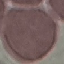

Result: no malaria parasites seen. Giemsa stain. Acquired by smartphone through the microscope eyepiece. Cell patch, automatically extracted from a larger field of view and resized to 64 × 64 pixels. Thin blood smear.